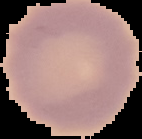

Result: no Plasmodium parasites seen. From a thin blood film. Segmented cell region on a black background. Image is 142×139 pixels.